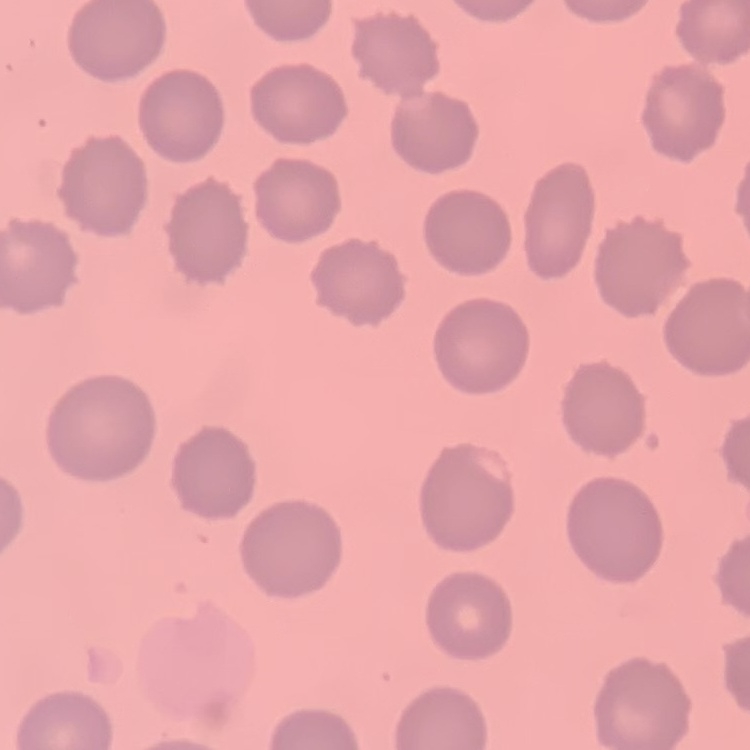

red blood cell morphology = no rouleaux formation
stain = Field's or Giemsa
preparation = thin blood film
image type = one tile cut from a larger photomicrograph